Give the position of every Plasmodium parasite visible.
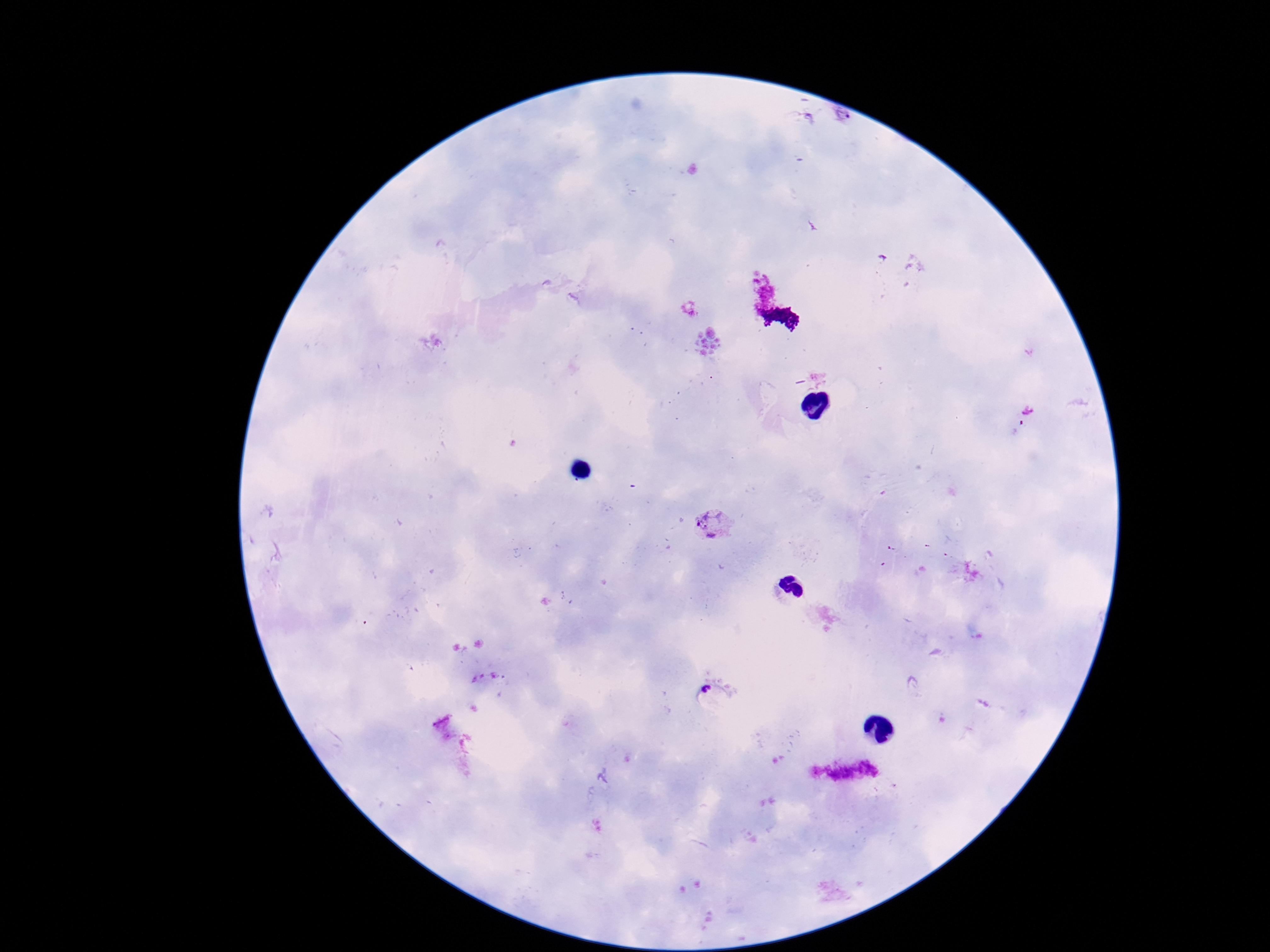

Approximate object centers, in pixels from the top-left corner.
Plasmodium parasites: (x=712, y=524).

Thick blood smear. One field from this slide. Image is 1270×952 pixels. Giemsa-stained preparation. Patient malaria status: infected. Smartphone photograph taken through the microscope eyepiece. 100x magnification.